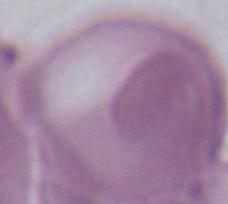

Summary:
  - Magnification: 1000x
  - Identification: red blood cell
  - Modality: photomicrograph